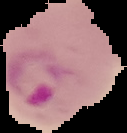

Summary:
  - Image size: 127×133 pixels
  - Malaria status: parasitized
  - Preparation: thin blood smear
  - Image type: segmented cell region on a black background